Assess the morphology of the erythrocytes.
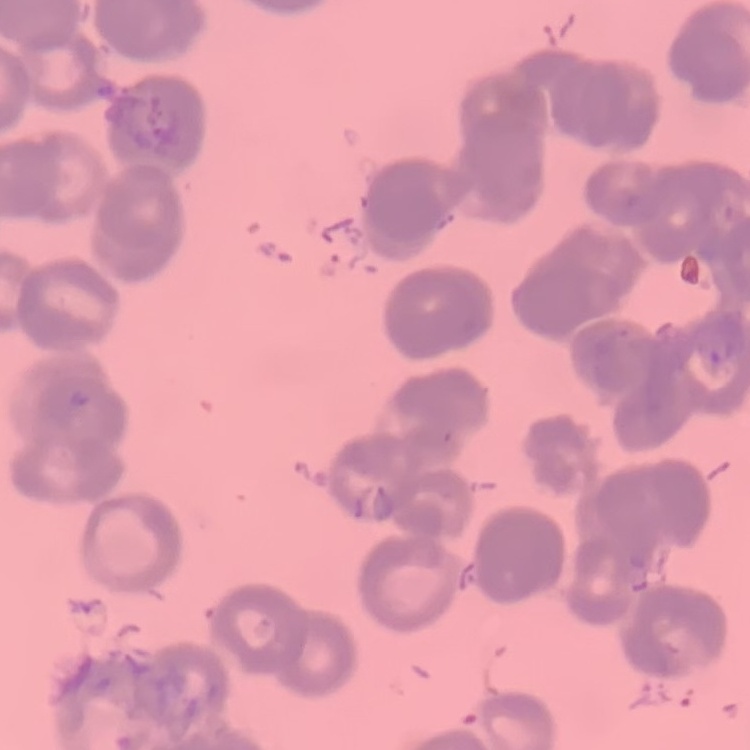
Rouleaux formation.

Summary:
  - Image type: one tile cut from a larger photomicrograph
  - Preparation: thin blood smear
  - Stain: Field's or Giemsa